Identify the preparation type.
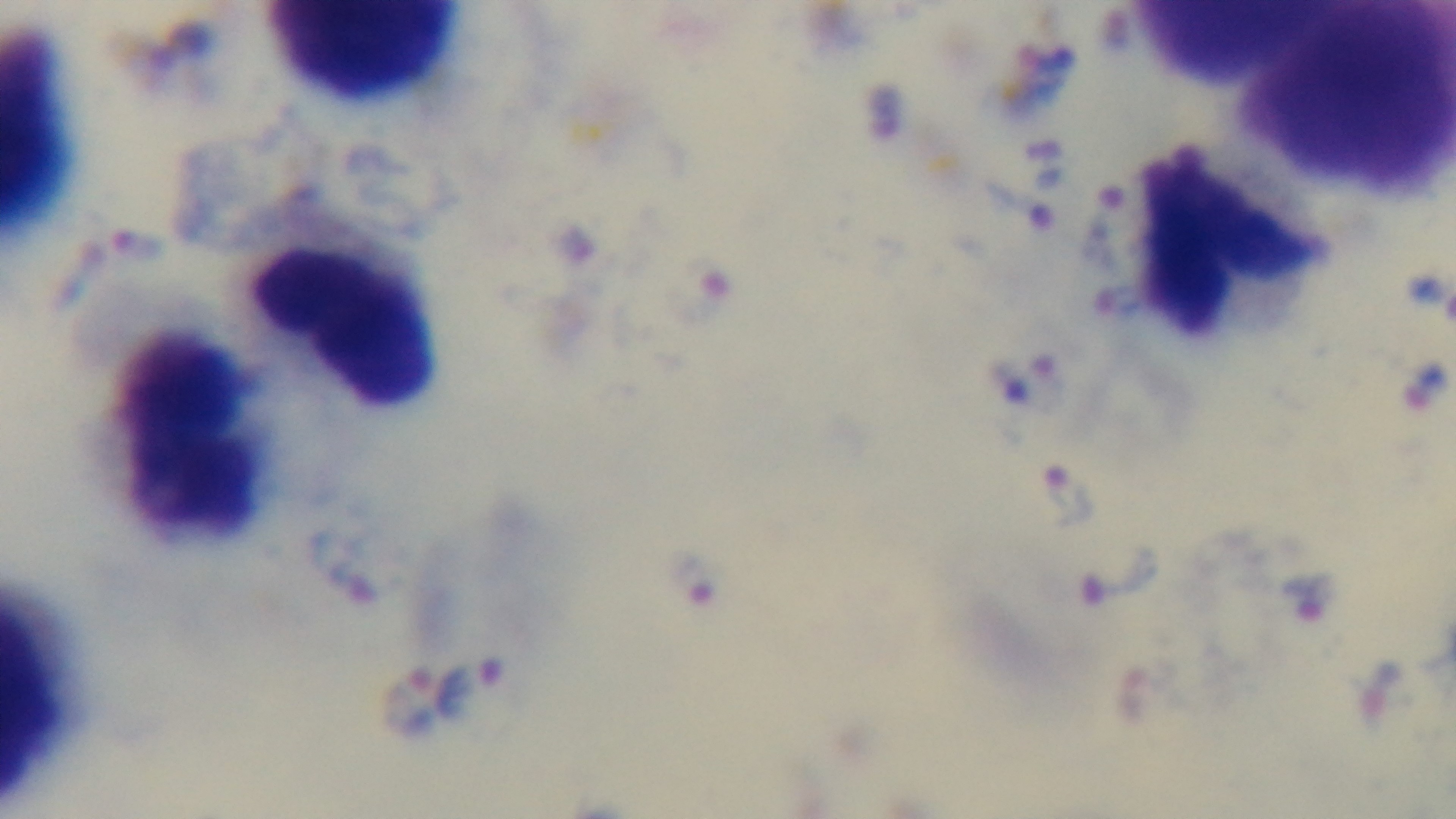

It is a thick blood film.

field of view = single
capture = mounted 4K digital camera
objective = 100x oil immersion
stain = Giemsa
modality = light microscopy
malaria status = positive